Point out each Plasmodium parasite.
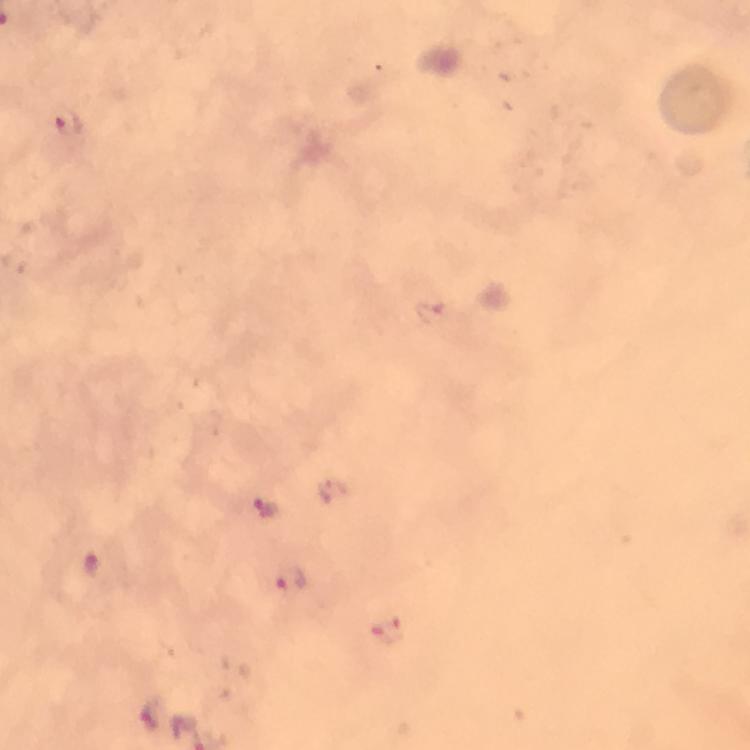

Approximate object centers, in pixels from the top-left corner.
Plasmodium parasites: (x=66, y=123), (x=429, y=312), (x=268, y=507), (x=90, y=565), (x=291, y=581), (x=387, y=629), (x=149, y=715).

Summary:
  - Capture: smartphone camera through the microscope
  - Stain: Giemsa
  - Magnification: 100x
  - Context: from a malaria diagnostic workup
  - Preparation: thick blood film
  - Image size: 750×750 pixels
  - Cropped from: one field of view
  - Immersion oil: used